Report the malaria status of this cell.
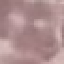
Uninfected.

stain = Giemsa
preparation = thin blood film
image type = cell patch, automatically extracted from a larger field of view and resized to 64 × 64 pixels
capture = smartphone through the microscope eyepiece